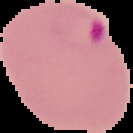
From a thin blood smear. Result: malaria parasites detected. Image is 133×133 pixels. The area outside the segmented cell region is set to black.